Assess this cell for malaria.
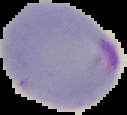

Parasitized.

Summary:
  - Image size: 127×115 pixels
  - Preparation: thin blood film
  - Image type: segmented cell region on a black background